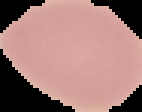

From a thin blood smear. The area outside the segmented cell region is set to black. Image is 142×112 pixels. Malaria status: uninfected.